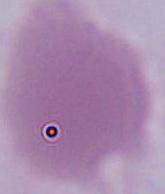

Captured at 1000x magnification. An erythrocyte is shown. Photomicrograph.